Identify the blood parasite species.
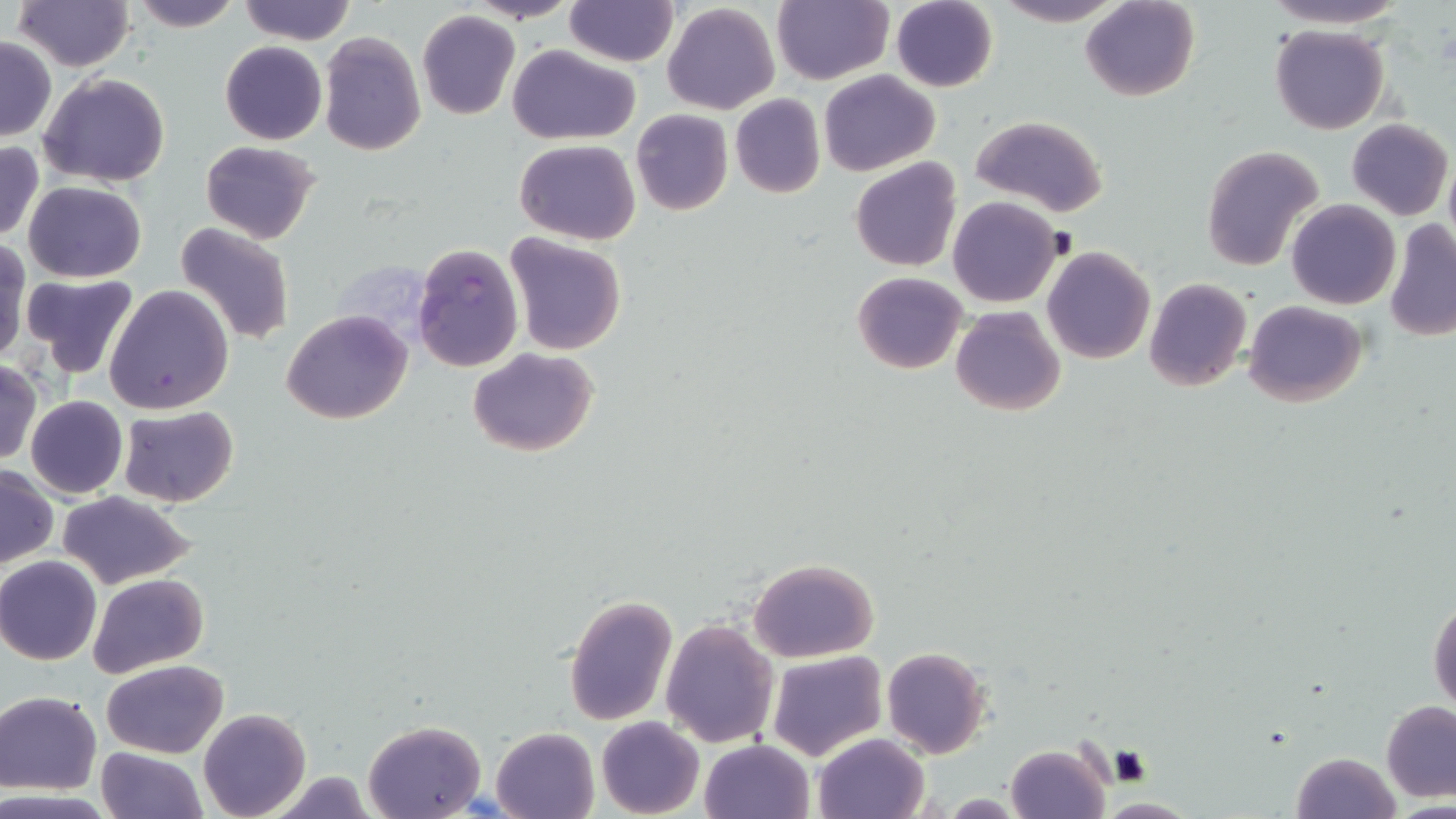

Plasmodium falciparum.

stain = May-Grünwald-Giemsa
image size = 1456×819 pixels
uninfected red blood cell locations = approximate bounding boxes as (x1, y1, x2, y2) in pixels: (11, 0, 133, 71), (128, 0, 243, 31), (238, 0, 357, 46), (470, 0, 578, 22), (564, 0, 678, 67), (772, 0, 892, 84), (994, 0, 1127, 26), (1081, 0, 1199, 102), (1262, 0, 1410, 28), (890, 1, 998, 92), (662, 2, 780, 113), (417, 11, 521, 120), (1270, 25, 1388, 135), (318, 32, 424, 156), (0, 36, 55, 141), (220, 41, 327, 146), (508, 45, 641, 144), (818, 69, 940, 177), (39, 72, 170, 186), (730, 94, 826, 199), (631, 109, 733, 215), (970, 115, 1109, 219), (1347, 120, 1453, 220), (514, 139, 640, 243), (198, 140, 321, 244), (0, 141, 46, 244), (1201, 146, 1325, 272), (850, 158, 962, 272), (1443, 159, 1456, 248), (23, 180, 147, 283), (948, 195, 1063, 308), (1286, 199, 1400, 311), (1384, 219, 1456, 341), (175, 220, 295, 347), (505, 233, 629, 355), (1, 238, 31, 367), (1042, 247, 1156, 365), (24, 271, 140, 377), (852, 271, 967, 375), (1144, 277, 1251, 392), (104, 285, 235, 415), (1244, 299, 1366, 406), (950, 305, 1066, 416), (282, 310, 411, 424), (466, 347, 599, 458), (0, 362, 41, 466), (25, 395, 128, 498), (117, 406, 238, 508), (1, 464, 58, 568), (56, 491, 197, 588), (0, 556, 103, 666), (747, 557, 879, 661), (87, 574, 209, 676), (564, 593, 677, 725), (1429, 596, 1456, 716), (661, 617, 779, 749), (882, 646, 991, 759), (766, 652, 886, 760), (103, 660, 228, 757), (0, 691, 100, 794), (1381, 700, 1456, 801), (199, 708, 310, 819), (596, 716, 704, 818), (361, 719, 487, 819), (492, 727, 598, 819), (813, 732, 930, 819), (700, 739, 813, 818), (1005, 743, 1112, 819), (96, 746, 207, 819), (1289, 751, 1401, 819), (262, 773, 379, 817)
Plasmodium falciparum-infected red blood cell locations = approximate bounding boxes as (x1, y1, x2, y2) in pixels: (412, 244, 523, 372)
modality = light microscopy
field of view = single
preparation = thin blood smear
magnification = 1000x